Give the preparation type.
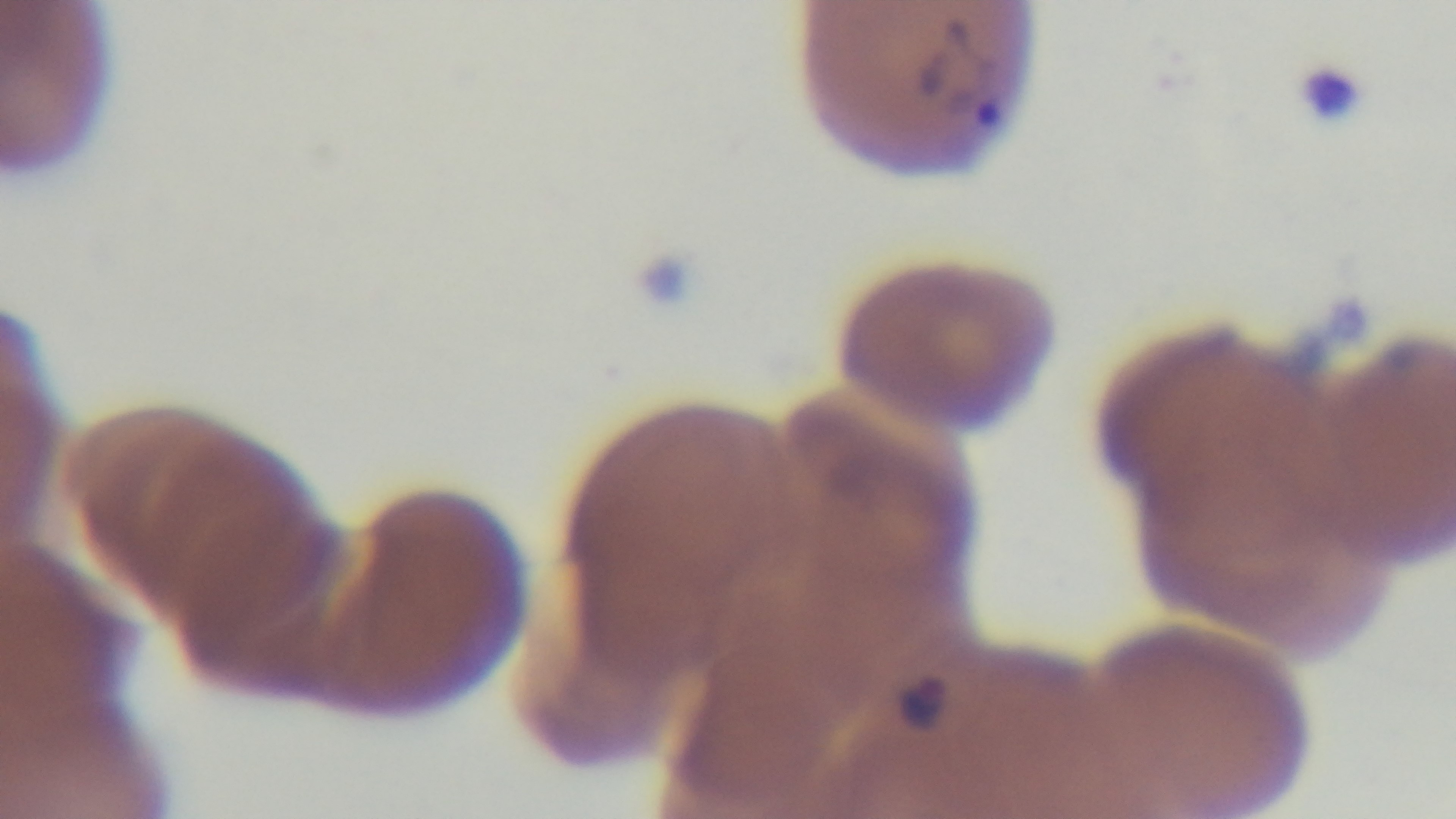
Thin.

Summary:
  - Malaria status: infected
  - Field of view: single
  - Modality: light microscopy
  - Objective: 100x oil immersion
  - Stain: Giemsa
  - Capture: mounted 4K digital camera